Assess this cell for malaria.
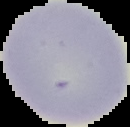
It is uninfected.

preparation = thin blood film
image type = segmented cell region on a black background
image size = 130×127 pixels